Assess the morphology of the erythrocytes.
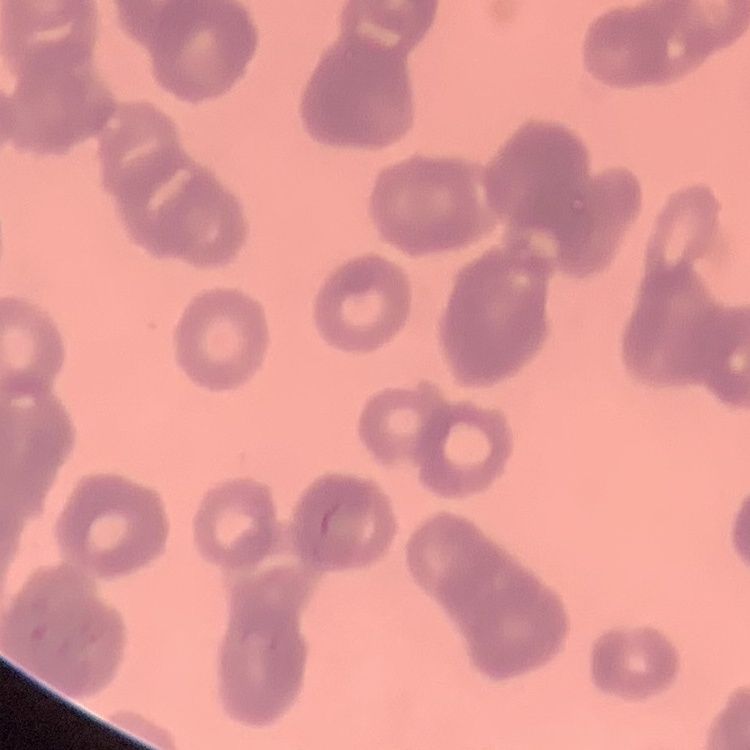

Rouleaux formation.

Field's or Giemsa stain. Thin peripheral smear. One tile cut from a larger photomicrograph.